Report the malaria status of this cell.
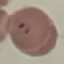

Parasitized.

capture = smartphone through the microscope eyepiece
stain = Giemsa
image type = cell patch, automatically extracted from a larger field of view and resized to 64 × 64 pixels
preparation = thin smear